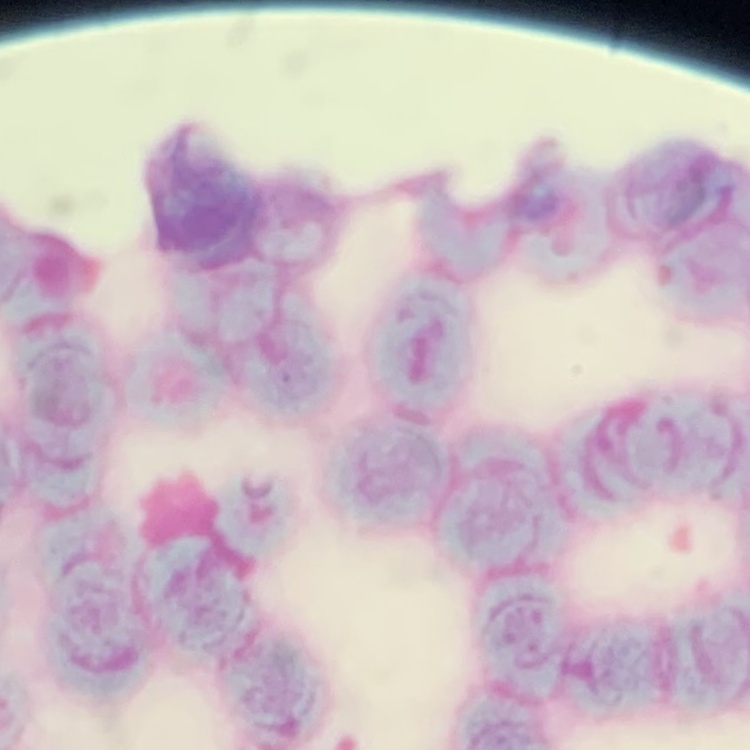

red blood cell morphology = rouleaux formation
stain = Field's or Giemsa
preparation = thin peripheral smear
image type = one tile cut from a larger photomicrograph